Classify this cell by malaria status.
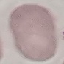
It is uninfected.

capture = smartphone camera at the microscope eyepiece
preparation = thin blood film
stain = Giemsa
image type = cell patch, automatically extracted from a larger field of view and resized to 64 × 64 pixels